Look for Plasmodium parasites.
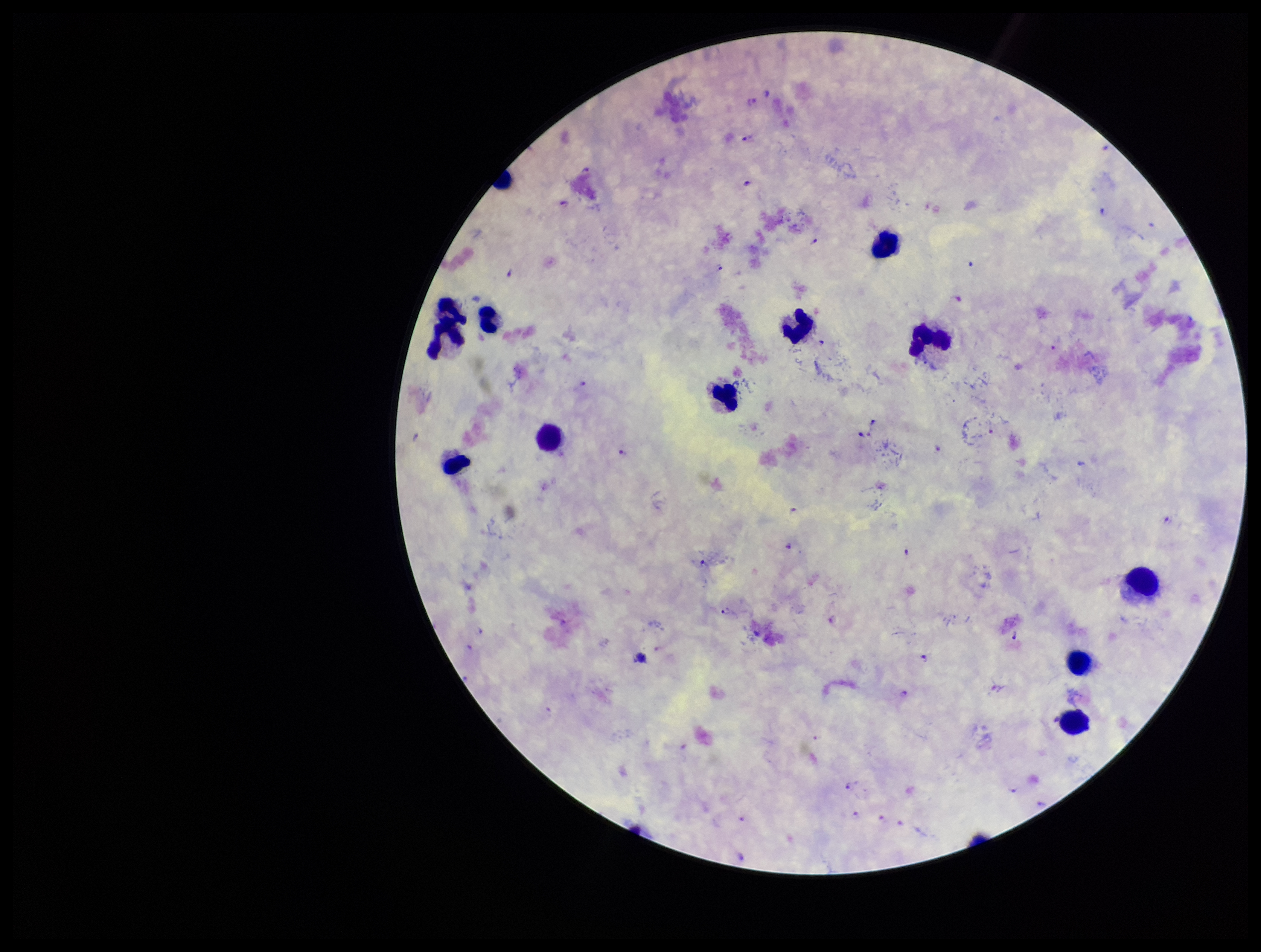

Seen.

Parasite count: 40. Patient malaria status: infected. Preparation: thick blood smear. Giemsa stain. Photographed through the microscope eyepiece with a smartphone camera. Image is 1261×952 pixels. One field from this slide. Species reported for this patient: Plasmodium falciparum. Leukocyte count: 11.